Classify this cell by malaria status.
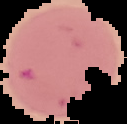
It is uninfected.

preparation = thin blood film
image type = cell region segmented out of the field of view; surrounding area masked to black
image size = 127×124 pixels